Name the cell type shown.
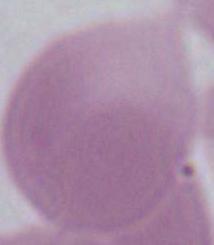

This is an erythrocyte.

Summary:
  - Magnification: 1000x
  - Modality: photomicrograph